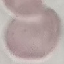
Result: no malaria parasites detected. Thin smear of blood. Giemsa stain. Photographed with a smartphone camera at the microscope eyepiece. Cell patch, automatically extracted from a larger field of view and resized to 64 × 64 pixels.